Classify this cell by malaria status.
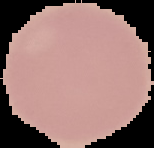

It is uninfected.

image size = 154×148 pixels
preparation = thin blood film
image type = cell region segmented out of the field of view; surrounding area masked to black